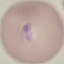
{
  "result": "malaria parasites detected",
  "preparation": "thin smear",
  "capture": "smartphone camera at the microscope eyepiece",
  "stain": "Giemsa",
  "image_type": "cell patch, automatically extracted from a larger field of view and resized to 64 × 64 pixels"
}